Evaluate for Plasmodium parasites.
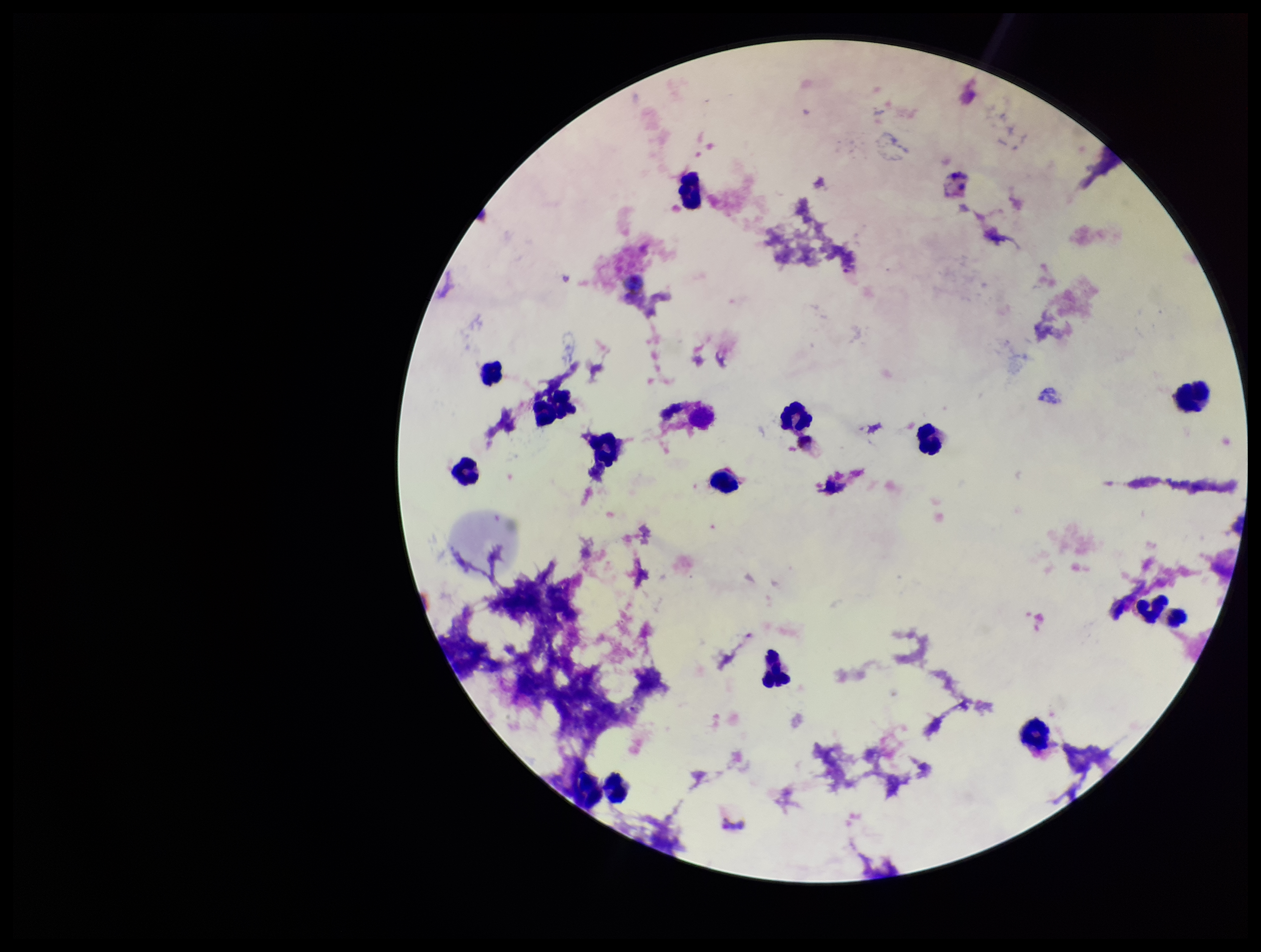
None seen.

One field from this slide. Preparation: thick blood smear. Image is 1261×952 pixels. Leukocyte count: 15. Smartphone photograph taken through the eyepiece of a microscope. Species reported for this patient: Plasmodium vivax. Stained with Giemsa. Patient malaria status: positive. Parasite count: 0.